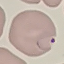

{
  "result": "malaria parasites detected",
  "capture": "smartphone camera at the microscope eyepiece",
  "stain": "Giemsa",
  "preparation": "thin blood film",
  "image_type": "cell patch, automatically extracted from a larger field of view and resized to 64 × 64 pixels"
}